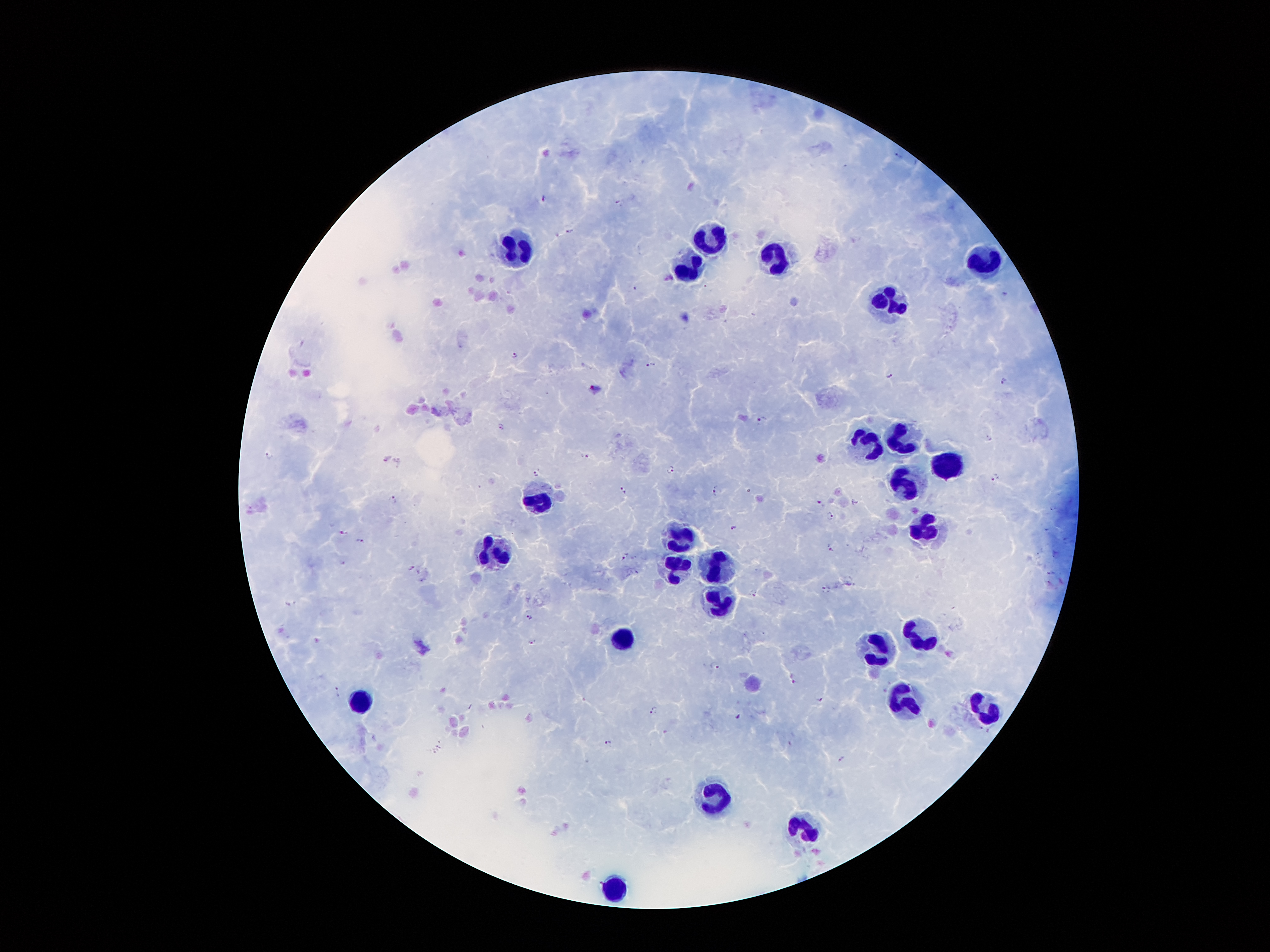
coordinate format = approximate centers as [x, y] in pixels
leukocyte locations = [708, 238], [516, 246], [774, 257], [986, 261], [689, 267], [888, 303], [902, 436], [869, 443], [949, 464], [904, 482], [534, 500], [929, 526], [680, 533], [498, 549], [675, 568], [718, 568], [725, 604], [922, 633], [622, 640], [882, 653], [362, 703], [906, 704], [984, 711], [714, 795], [808, 830], [610, 890]
Plasmodium parasite locations = [899, 155], [543, 198], [620, 200], [569, 230], [1005, 293], [514, 354], [651, 364], [890, 374], [1003, 379], [595, 387], [762, 419], [502, 425], [268, 454], [587, 455], [670, 470], [535, 473], [993, 476], [622, 490], [715, 491], [393, 498], [819, 502], [832, 512], [733, 527], [343, 531], [360, 540], [831, 545], [625, 556], [343, 562], [410, 567], [825, 588], [289, 602], [531, 616], [532, 642], [715, 664], [793, 681], [337, 689], [819, 698], [653, 709], [737, 717], [608, 742], [440, 743], [434, 751], [841, 759]
stain = Giemsa
patient malaria status = positive for Plasmodium falciparum
image size = 1270×952 pixels
capture = smartphone camera through the microscope eyepiece
magnification = 100x
field of view = single
preparation = thick blood film